Locate every blood parasite and identify its species.
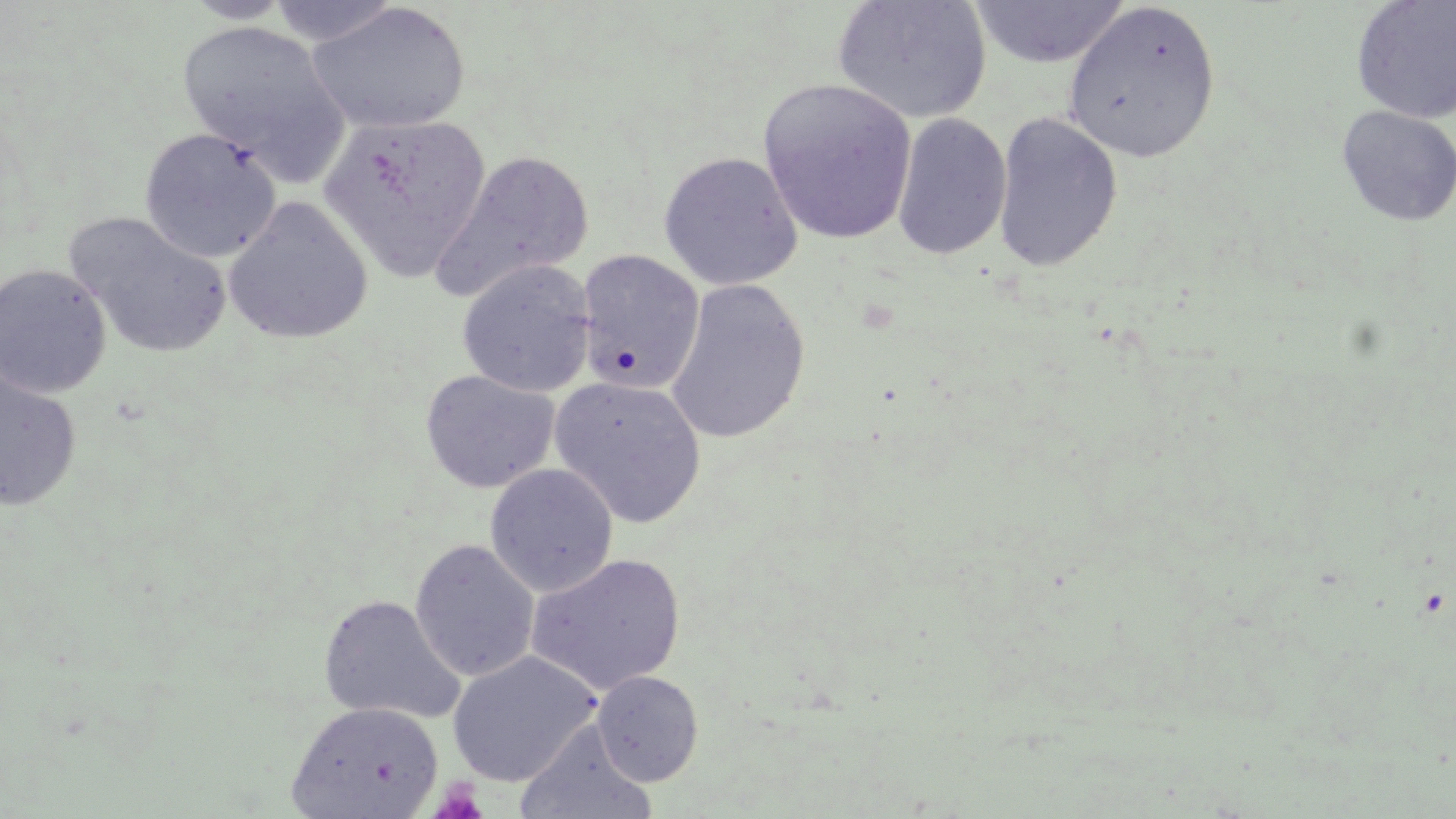
No blood parasites observed.

Summary:
  - Coordinate format: approximate bounding boxes as [x1, y1, x2, y2] in pixels
  - Platelet locations: [430, 781, 489, 819]
  - Uninfected red blood cell locations: [181, 0, 296, 24], [831, 0, 992, 124], [1351, 0, 1456, 124], [266, 1, 402, 47], [969, 1, 1131, 68], [307, 2, 471, 135], [1062, 2, 1221, 164], [177, 20, 349, 176], [758, 79, 916, 245], [1336, 105, 1455, 227], [318, 112, 490, 283], [993, 112, 1123, 274], [892, 113, 1012, 262], [139, 127, 281, 264], [433, 151, 594, 301], [658, 151, 803, 290], [223, 196, 373, 345], [64, 212, 232, 360], [576, 250, 705, 394], [456, 260, 596, 397], [0, 264, 112, 398], [665, 280, 811, 444], [0, 364, 82, 513], [420, 369, 560, 494], [549, 376, 707, 527], [484, 464, 618, 597], [409, 539, 540, 683], [526, 553, 686, 696], [318, 594, 465, 724], [446, 651, 601, 787], [592, 670, 704, 786], [287, 701, 443, 818], [516, 722, 656, 819]
  - Slide-level diagnosis: negative for blood parasites
  - Magnification: 1000x
  - Preparation: thin blood smear
  - Modality: optical microscopy
  - Field of view: single
  - Image size: 1456×819 pixels
  - Stain: May-Grünwald-Giemsa